Give the position of every Plasmodium parasite visible.
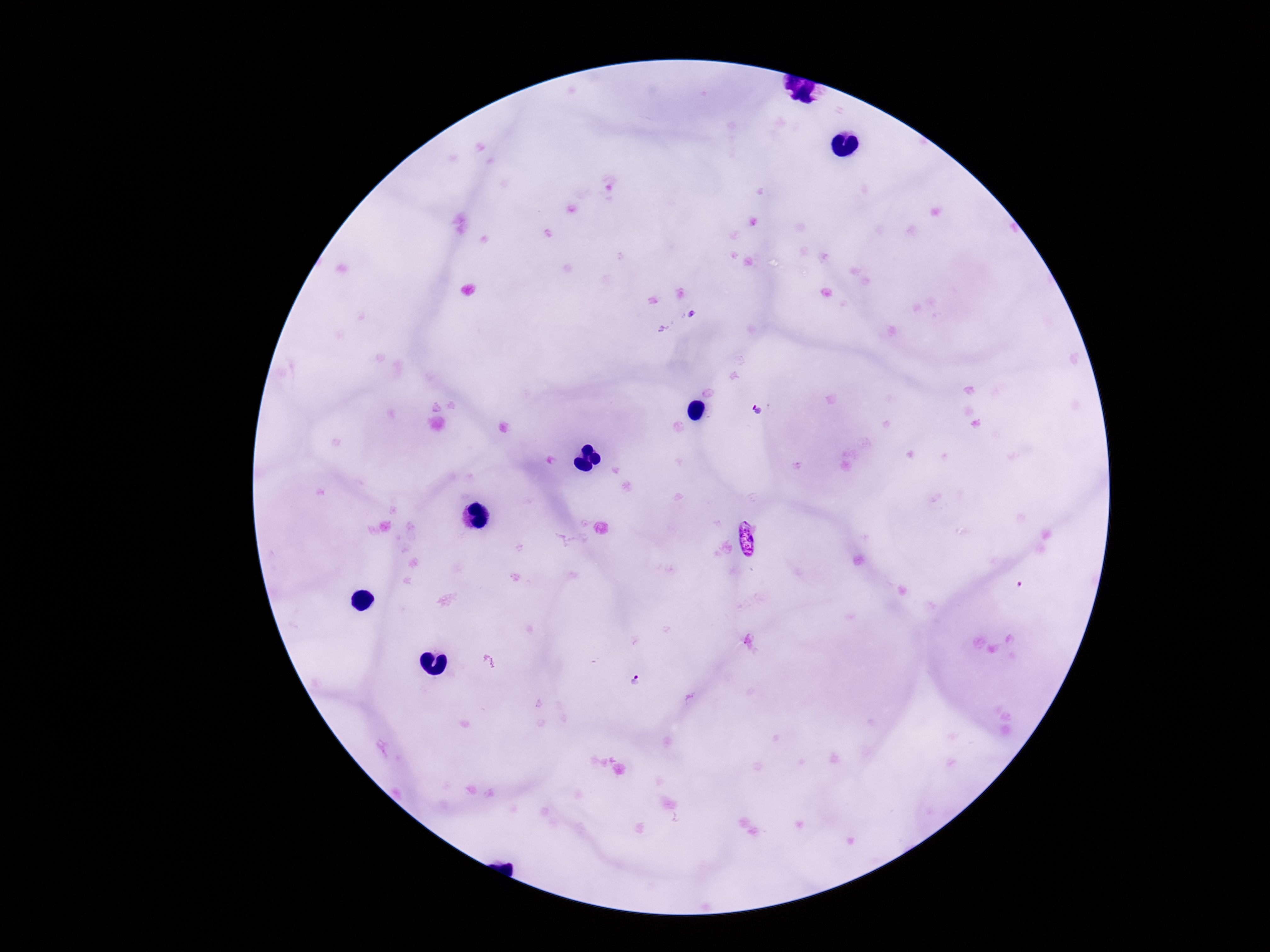

Approximate centers as [x, y] in pixels.
Plasmodium parasites: [761, 411], [638, 680].

Summary:
  - Stain: Giemsa
  - Field of view: single
  - Image size: 1270×952 pixels
  - Preparation: thick blood smear
  - Magnification: 100x
  - Capture: smartphone camera through the microscope eyepiece
  - Patient malaria status: positive